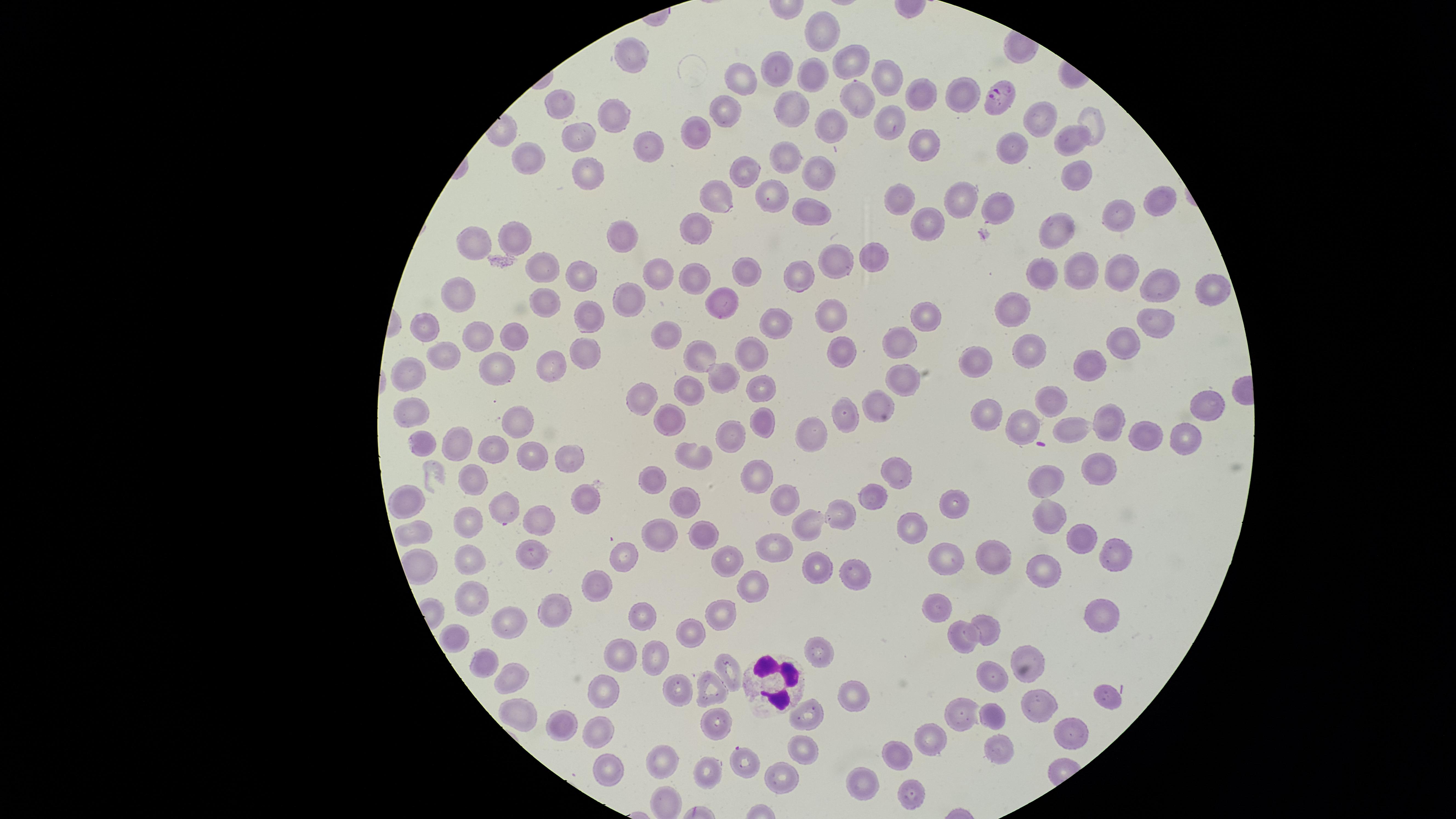 Approximate marker points as [x, y] in pixels. Parasitized RBCs: [997, 96], [742, 759]. WBCs: [767, 681]. Uninfected RBCs: [823, 31], [634, 54], [854, 64], [778, 70], [812, 74], [744, 76], [894, 78], [960, 94], [924, 97], [862, 99], [727, 102], [561, 104], [794, 109], [617, 114], [1044, 117], [1094, 119], [887, 124], [702, 127], [830, 127], [583, 136], [1074, 139], [1012, 143], [919, 145], [653, 150], [530, 156], [790, 157], [747, 164], [816, 169], [591, 171], [1075, 175], [714, 193], [769, 194], [904, 197], [958, 198], [1153, 199], [1006, 207], [805, 211], [1112, 213], [699, 223], [924, 225], [1061, 230], [626, 235], [518, 236], [477, 244], [873, 258], [841, 259], [658, 266], [542, 269], [1080, 269], [1111, 270], [747, 273], [803, 273], [1036, 273], [694, 276], [581, 277], [1159, 280], [458, 287], [1207, 288], [632, 293], [545, 300], [728, 303], [1015, 309], [830, 313], [924, 316], [776, 318], [590, 320], [1152, 321], [428, 326], [478, 333], [668, 333], [518, 334], [1126, 342], [902, 343], [588, 349], [843, 352], [1026, 352], [707, 354], [750, 354], [975, 357], [447, 359], [1086, 362], [497, 367], [552, 367], [414, 372], [724, 375], [899, 377], [757, 385], [689, 387], [645, 392], [1047, 396], [880, 399], [1204, 401], [410, 409], [984, 412], [843, 413], [519, 414], [765, 418], [1024, 421], [1105, 421], [667, 422], [1069, 428], [812, 430], [729, 432], [1182, 435], [1141, 436], [423, 441], [459, 442], [494, 450], [529, 455], [571, 457], [698, 458], [1106, 469], [899, 472], [760, 477], [656, 478], [470, 483], [1053, 483], [876, 494], [409, 497], [955, 499], [689, 501], [782, 501], [578, 502], [509, 506], [838, 509], [1047, 510], [472, 519], [815, 524], [536, 525], [913, 526], [417, 531], [665, 533], [704, 534], [1077, 538], [776, 546], [627, 552], [1115, 554], [532, 555], [944, 555], [727, 557], [1000, 559], [476, 560], [818, 564], [1048, 571], [852, 578], [595, 584], [758, 589], [475, 599], [940, 606], [1099, 607], [555, 608], [725, 613], [646, 616], [511, 622], [692, 627], [987, 627], [458, 635], [962, 638], [820, 646], [617, 657], [1032, 657], [492, 661], [653, 663], [729, 664], [997, 675], [512, 676], [682, 689], [711, 689], [1102, 693], [605, 696], [854, 696], [1043, 704], [521, 711], [808, 713], [993, 714], [962, 718], [718, 721], [563, 724], [599, 729], [1073, 729], [930, 736], [996, 751], [805, 752], [896, 754], [664, 761], [612, 763], [703, 768], [784, 780], [868, 783], [907, 790]. Smartphone photograph through the microscope eyepiece. Giemsa-stained preparation. Species: Plasmodium falciparum. One field of view of the specimen. Thin blood film. Circular visible region. Image is 1456×819 pixels. Presence: malaria parasites detected.